Point out each leukocyte.
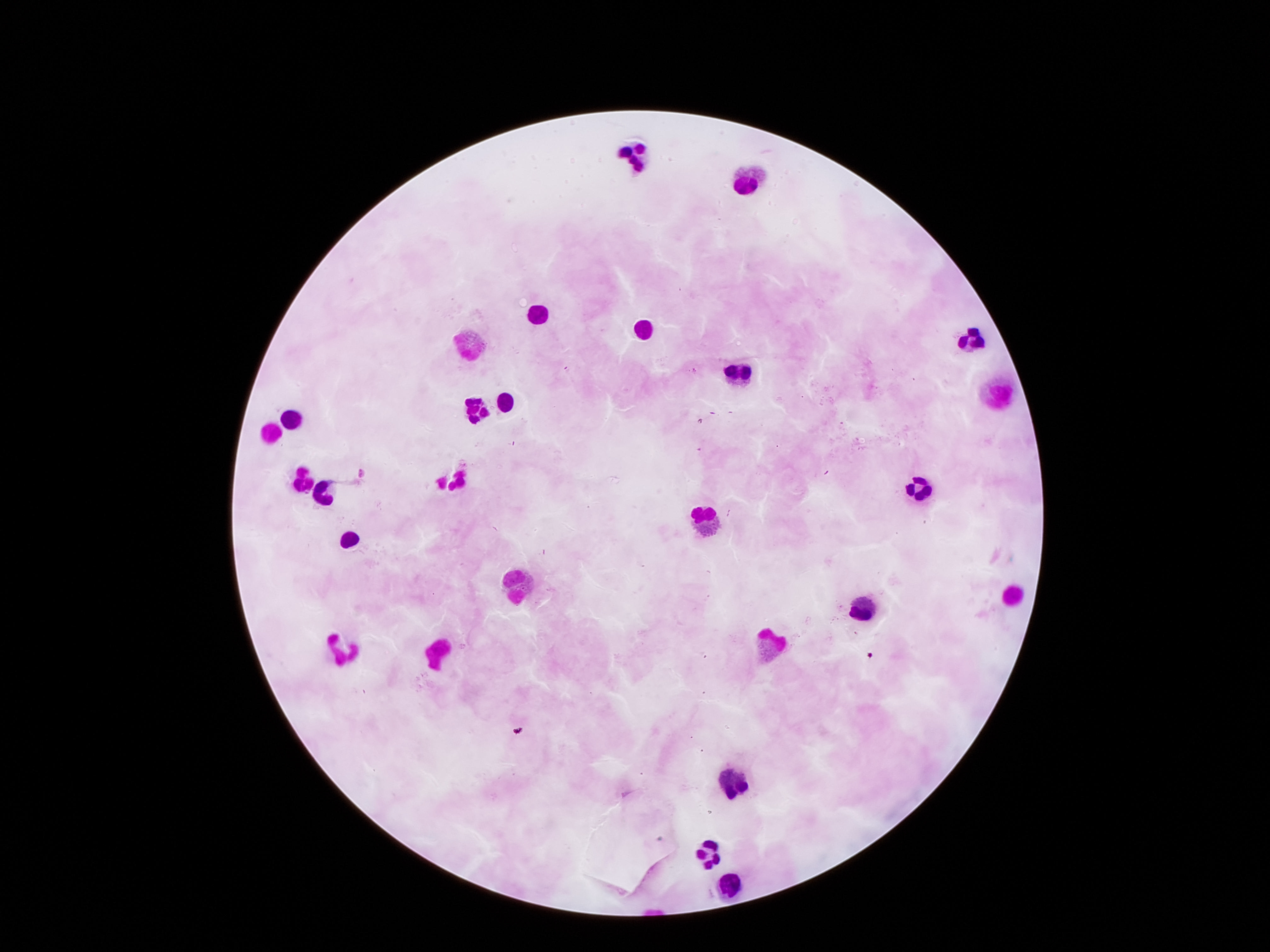
Approximate object centers, in pixels from the top-left corner.
Leukocytes: (x=631, y=159), (x=745, y=171), (x=537, y=308), (x=646, y=326), (x=969, y=339), (x=466, y=342), (x=743, y=370), (x=997, y=391), (x=507, y=399), (x=474, y=410), (x=295, y=418), (x=273, y=431), (x=299, y=476), (x=453, y=476), (x=923, y=492), (x=326, y=495), (x=709, y=518), (x=352, y=540), (x=519, y=579), (x=1016, y=596), (x=865, y=611), (x=767, y=641), (x=345, y=649), (x=441, y=654), (x=735, y=778), (x=710, y=854), (x=733, y=887).

{
  "patient_malaria_status": "negative",
  "magnification": "100x",
  "capture": "smartphone camera through the microscope eyepiece",
  "image_size": "1270×952 pixels",
  "preparation": "thick peripheral-blood smear",
  "field_of_view": "one from this slide",
  "stain": "Giemsa"
}